Assess this cell for malaria.
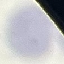
It is uninfected.

image type = automatically extracted cell patch, resized to 64 × 64 pixels
capture = smartphone through the microscope eyepiece
preparation = thin smear
stain = Giemsa